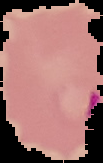
From a thin blood film. Cell region segmented out of the field of view; the surrounding area is masked to black. Malaria status: parasitized. Image is 103×163 pixels.